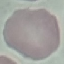
Result: negative for malaria parasites. Thin blood smear. Photographed with a smartphone camera at the microscope eyepiece. Giemsa-stained preparation. Cell patch, automatically extracted from a larger field of view and resized to 64 × 64 pixels.